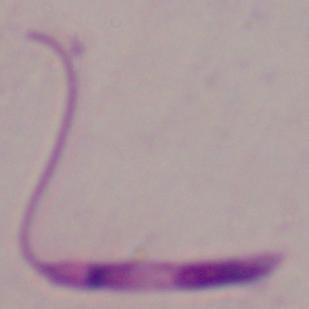 Captured at 1000x magnification. Photomicrograph. A Leishmania parasite is shown.